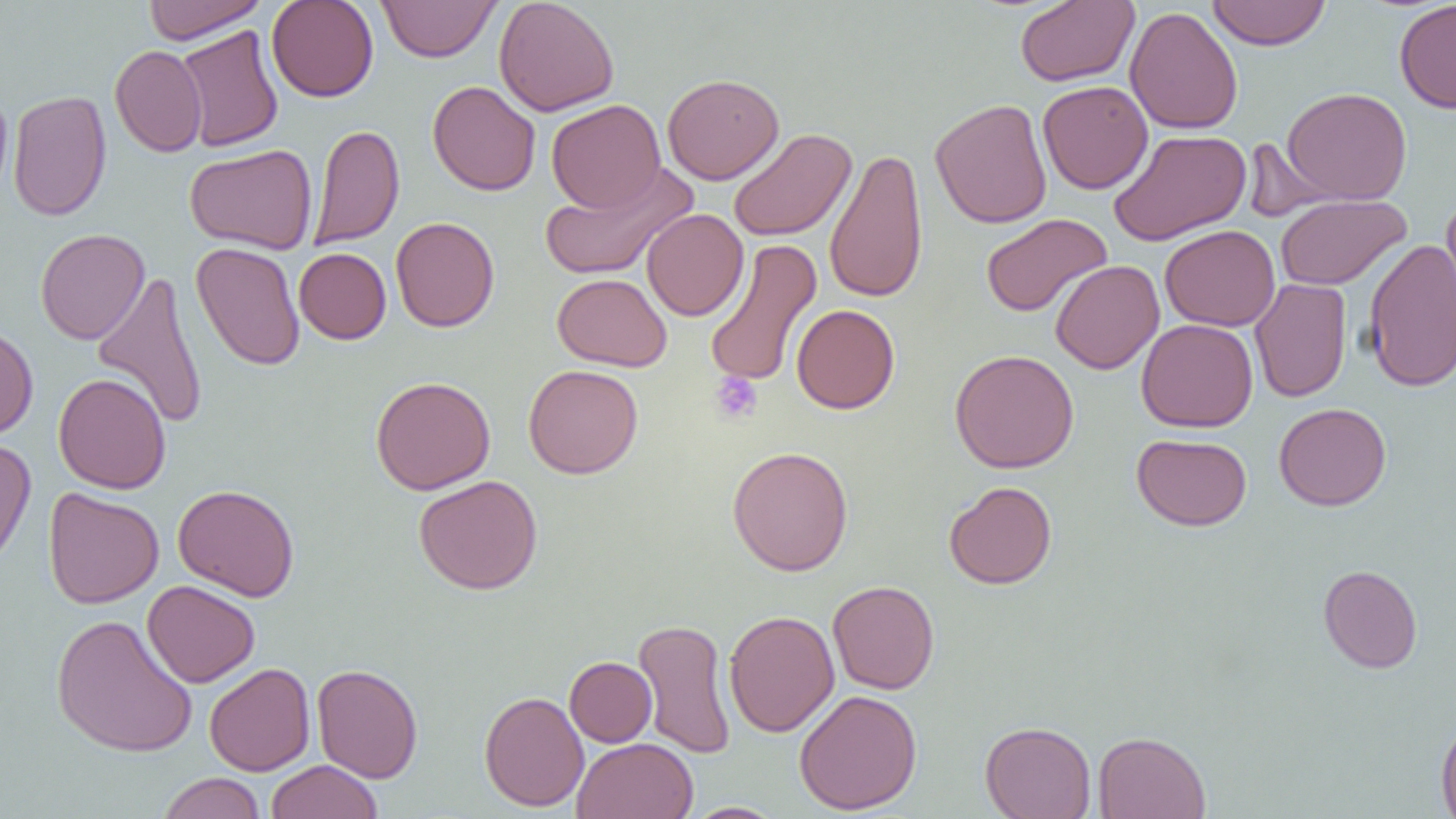 Approximate bounding boxes as (x1,y1)-(x2,y2) corner pairs in pixels. Uninfected red blood cell locations: (143,0)-(267,44), (267,0)-(379,102), (377,0)-(500,63), (494,0)-(620,116), (1206,0)-(1331,50), (1394,0)-(1456,114), (1015,1)-(1139,87), (1125,6)-(1243,135), (174,24)-(284,153), (110,45)-(207,157), (662,73)-(784,185), (427,80)-(541,196), (1037,80)-(1153,194), (0,86)-(13,204), (1281,87)-(1412,205), (7,90)-(112,221), (930,98)-(1052,229), (546,99)-(666,213), (309,124)-(404,250), (727,128)-(857,242), (1108,129)-(1252,246), (1240,137)-(1343,223), (185,144)-(317,254), (824,146)-(929,304), (539,161)-(698,282), (1275,194)-(1411,290), (1441,196)-(1456,314), (641,209)-(749,321), (981,213)-(1112,318), (390,216)-(500,333), (1160,225)-(1280,331), (35,228)-(150,344), (1363,237)-(1456,393), (704,238)-(822,389), (190,241)-(305,371), (293,242)-(499,337), (294,248)-(391,344), (1050,260)-(1165,374), (91,271)-(209,430), (552,273)-(672,372), (1249,278)-(1352,403), (791,304)-(900,414), (1136,318)-(1258,433), (0,325)-(38,440), (950,349)-(1079,473), (523,364)-(644,479), (53,372)-(171,494), (370,376)-(495,495), (1274,402)-(1391,511), (1132,433)-(1251,531), (0,437)-(36,571), (727,445)-(854,576), (413,475)-(543,595), (943,480)-(1057,589), (172,483)-(300,602), (43,488)-(164,608), (1318,564)-(1423,673), (142,580)-(260,688), (827,580)-(940,695), (724,609)-(839,737), (50,613)-(198,758), (632,618)-(737,759), (565,656)-(657,747), (204,663)-(315,776), (312,663)-(423,783), (794,689)-(922,815), (479,690)-(589,811), (1435,717)-(1456,818), (980,721)-(1096,819), (1093,730)-(1211,819), (571,737)-(698,819), (266,760)-(383,819), (158,772)-(266,819), (683,802)-(788,819). Platelet locations: (709,372)-(763,424). Slide-level diagnosis: negative for blood parasites. Image is 1456×819 pixels. Light microscopy. One field of a larger specimen. Thin blood smear. Captured at 1000x magnification.